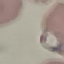 Malaria status: parasitized. Cell patch, automatically extracted from a larger field of view and resized to 64 × 64 pixels. Thin blood film. Giemsa-stained preparation. Photographed with a smartphone camera at the microscope eyepiece.